Report the malaria status of this cell.
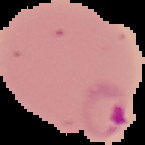

It is parasitized.

Image is 145×145 pixels. From a thin blood smear. Segmented cell region on a black background.